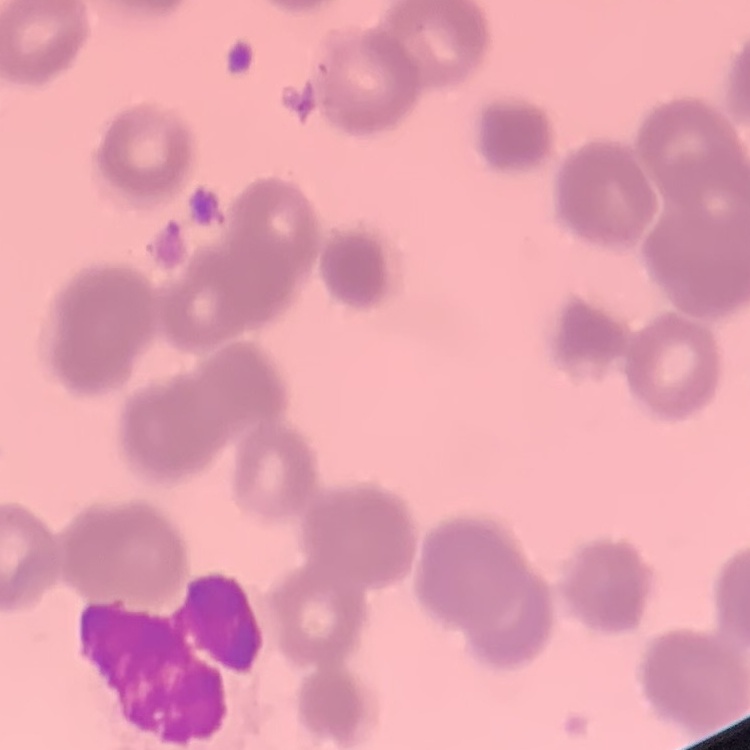
Summary:
  - Red blood cell morphology: rouleaux formation
  - Preparation: thin blood film
  - Stain: Field's or Giemsa
  - Image type: square crop of a larger photomicrograph